Report the malaria status of this cell.
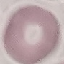
Uninfected.

{
  "image_type": "automatically extracted cell patch, resized to 64 × 64 pixels",
  "preparation": "thin blood film",
  "capture": "smartphone through the microscope eyepiece",
  "stain": "Giemsa"
}